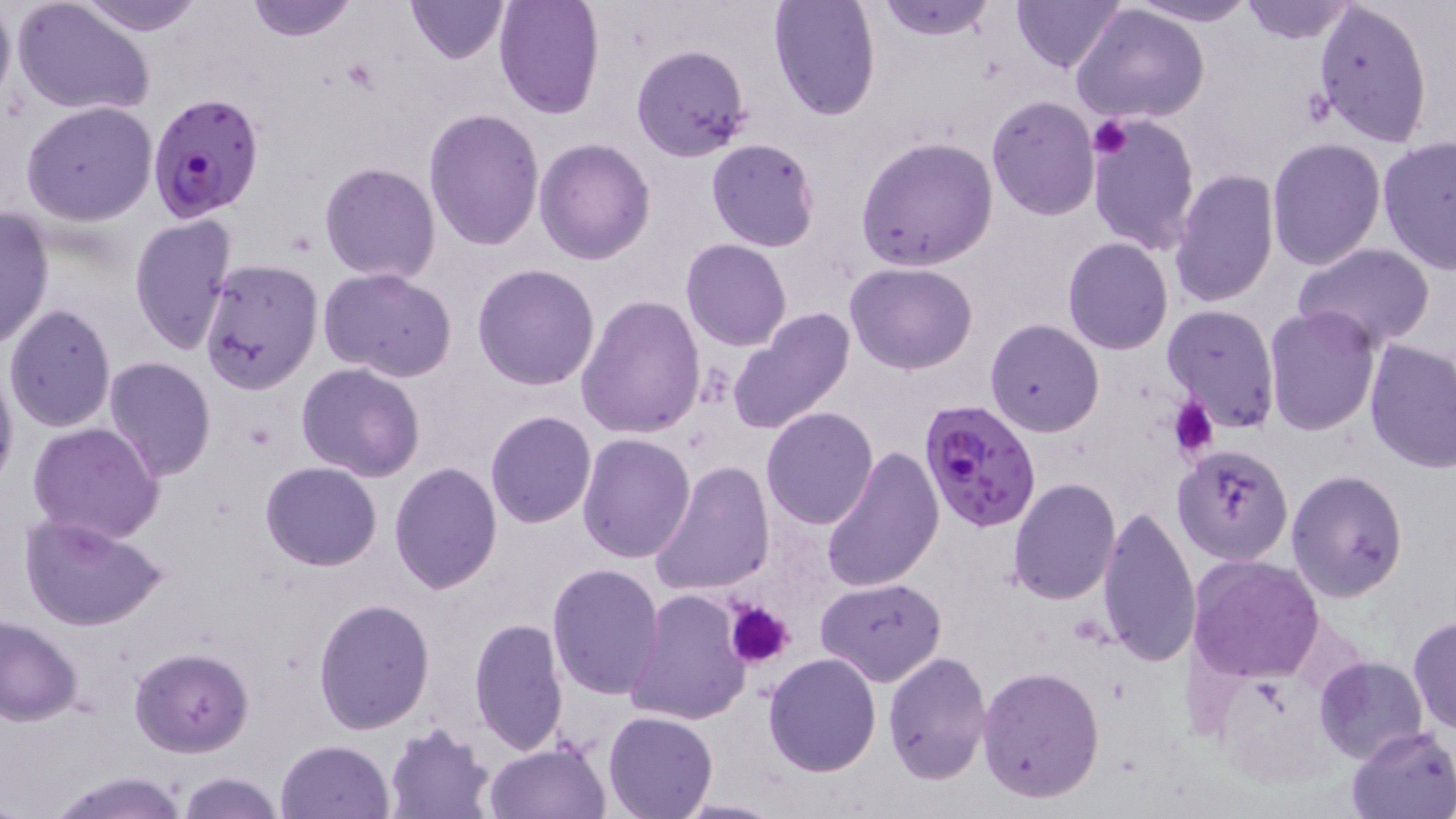
Approximate bounding boxes as [x1, y1, x2, y2] in pixels. Plasmodium falciparum-infected red blood cell locations: [148, 92, 267, 222], [917, 397, 1044, 534]. Platelet locations: [1088, 115, 1136, 158], [1167, 398, 1219, 460], [725, 601, 796, 669]. Uninfected red blood cell locations: [0, 0, 14, 116], [11, 0, 154, 119], [71, 0, 207, 35], [243, 0, 359, 42], [404, 0, 510, 63], [492, 0, 606, 120], [769, 0, 881, 120], [870, 0, 999, 42], [1011, 0, 1126, 75], [1122, 0, 1262, 26], [1235, 1, 1360, 44], [1314, 1, 1434, 147], [1071, 5, 1211, 127], [632, 44, 752, 163], [986, 96, 1100, 219], [20, 100, 159, 226], [424, 107, 545, 251], [1084, 110, 1200, 254], [1376, 135, 1456, 274], [855, 136, 999, 271], [1265, 136, 1385, 270], [535, 137, 655, 264], [706, 138, 820, 252], [319, 162, 440, 283], [1170, 167, 1280, 309], [0, 206, 54, 350], [128, 213, 238, 356], [1062, 237, 1173, 355], [681, 239, 791, 350], [1292, 243, 1437, 351], [199, 259, 323, 394], [844, 261, 979, 374], [471, 264, 601, 391], [319, 269, 458, 383], [577, 294, 707, 438], [4, 303, 118, 431], [1162, 304, 1282, 433], [1262, 304, 1382, 435], [725, 310, 857, 434], [985, 318, 1104, 437], [1363, 340, 1455, 473], [102, 357, 216, 481], [0, 359, 18, 495], [295, 363, 425, 481], [761, 407, 880, 529], [485, 410, 597, 529], [28, 422, 164, 544], [577, 433, 696, 564], [1172, 444, 1294, 566], [821, 446, 944, 595], [651, 459, 774, 596], [260, 461, 381, 570], [389, 461, 502, 592], [1285, 469, 1410, 602], [1007, 479, 1122, 605], [1096, 503, 1200, 669], [18, 513, 170, 633], [1103, 523, 1310, 674], [1187, 554, 1326, 683], [546, 563, 665, 700], [816, 577, 948, 686], [624, 588, 751, 726], [313, 598, 435, 734], [1408, 615, 1456, 733], [0, 616, 83, 724], [469, 618, 568, 757], [129, 647, 254, 756], [881, 651, 992, 785], [762, 653, 884, 776], [1314, 655, 1428, 762], [977, 666, 1106, 803], [604, 709, 718, 818], [384, 725, 497, 818], [1347, 727, 1456, 818], [275, 739, 397, 819], [484, 742, 611, 819], [44, 769, 194, 819], [175, 773, 286, 819], [669, 798, 785, 817]. Slide-level diagnosis: Plasmodium falciparum. One field of a larger specimen. Captured at 1000x magnification. May-Grünwald-Giemsa-stained preparation. Optical microscopy. Image is 1456×819 pixels. Thin blood film.